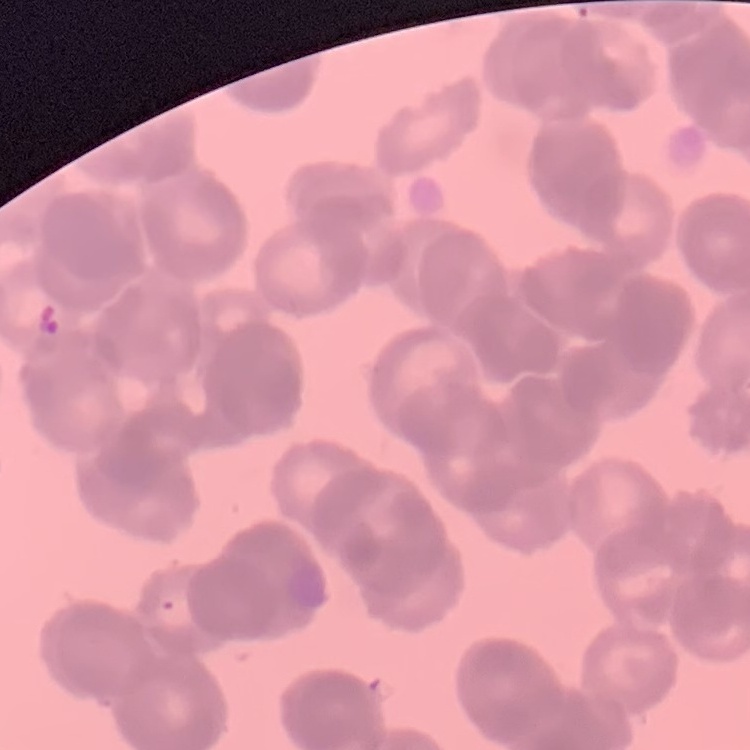
red_blood_cell_morphology: rouleaux formation
stain: Field's or Giemsa
image_type: one tile cut from a larger photomicrograph
preparation: thin blood film